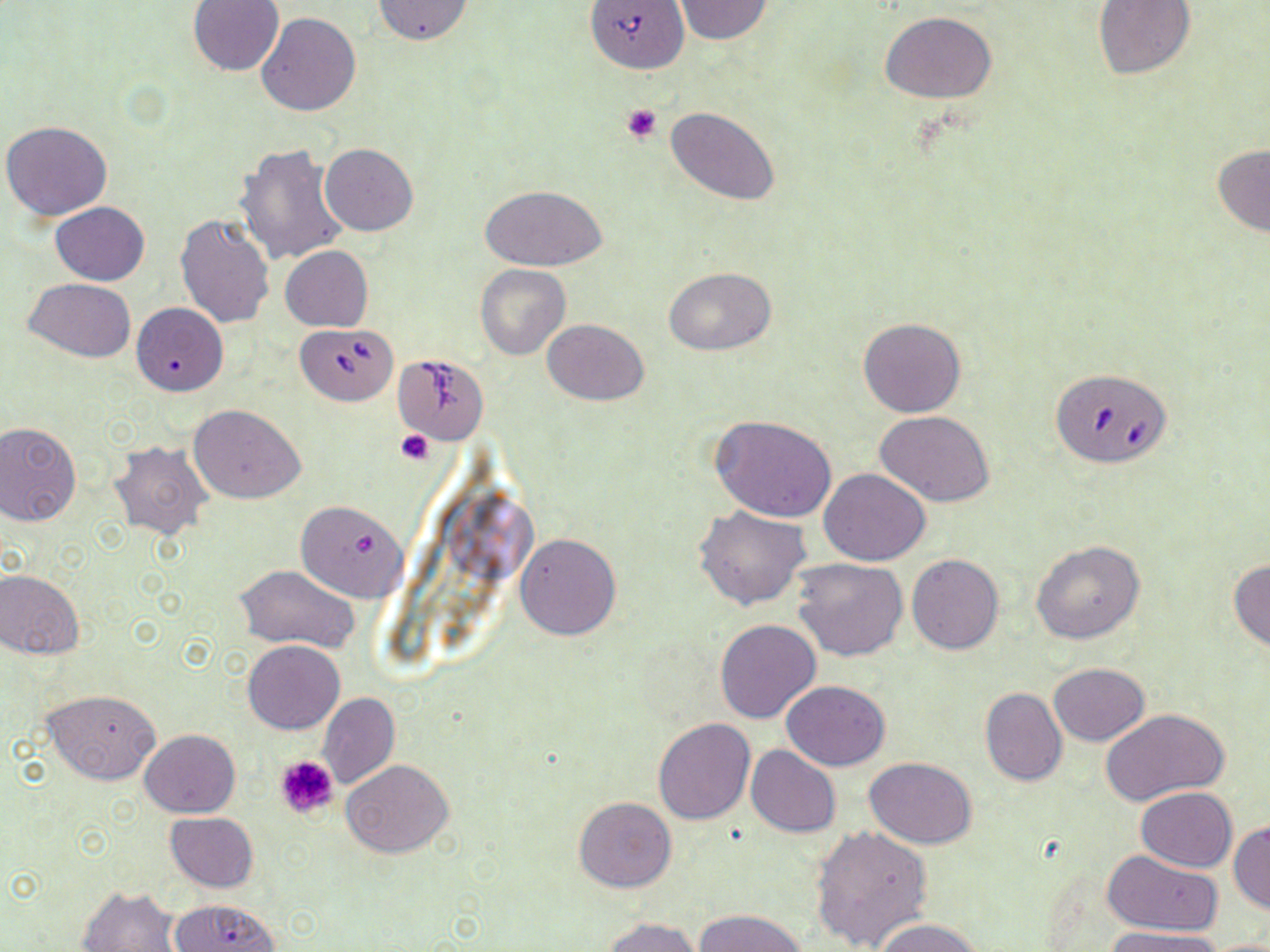
Approximate bounding boxes as [x1, y1, x2, y2] in pixels. Uninfected red blood cell locations: [186, 0, 283, 76], [371, 0, 476, 46], [674, 0, 773, 44], [1092, 0, 1195, 79], [882, 12, 997, 103], [257, 13, 361, 117], [664, 107, 780, 204], [2, 119, 112, 220], [320, 143, 417, 235], [236, 144, 349, 267], [1212, 145, 1270, 235], [480, 184, 608, 271], [52, 202, 150, 285], [176, 214, 275, 328], [280, 245, 373, 332], [475, 264, 572, 360], [663, 266, 775, 355], [25, 277, 135, 361], [132, 302, 227, 396], [858, 317, 967, 417], [542, 318, 648, 406], [189, 404, 305, 504], [876, 410, 995, 507], [712, 416, 836, 523], [0, 422, 82, 525], [109, 441, 213, 539], [821, 468, 930, 565], [295, 500, 408, 602], [694, 506, 813, 611], [514, 532, 621, 640], [1031, 540, 1145, 644], [907, 555, 1003, 656], [792, 558, 908, 661], [1228, 559, 1270, 653], [234, 564, 358, 652], [0, 569, 84, 659], [715, 620, 821, 724], [243, 641, 345, 733], [1049, 663, 1149, 745], [781, 680, 890, 770], [980, 686, 1067, 786], [44, 688, 161, 785], [317, 692, 399, 790], [1102, 708, 1228, 807], [653, 718, 754, 824], [138, 729, 240, 818], [746, 744, 842, 837], [864, 758, 979, 848], [342, 759, 454, 858], [1135, 786, 1236, 871], [575, 797, 676, 892], [165, 812, 258, 892], [1229, 819, 1270, 913], [811, 825, 934, 952], [1104, 850, 1223, 935], [77, 886, 184, 952], [169, 899, 282, 951], [696, 908, 809, 952], [601, 916, 701, 952], [874, 917, 984, 952], [1103, 927, 1228, 952], [1206, 936, 1270, 952]. Babesia divergens-infected red blood cell locations: [584, 0, 689, 74], [296, 324, 396, 405], [390, 353, 491, 445], [1050, 367, 1173, 468]. Platelet locations: [622, 104, 662, 143], [396, 429, 434, 467], [272, 753, 339, 820]. Slide-level diagnosis: Babesia divergens. Light microscopy. May-Grünwald-Giemsa stain. Image is 1270×952 pixels. Single field of view. 1000x magnification. Thin blood film.